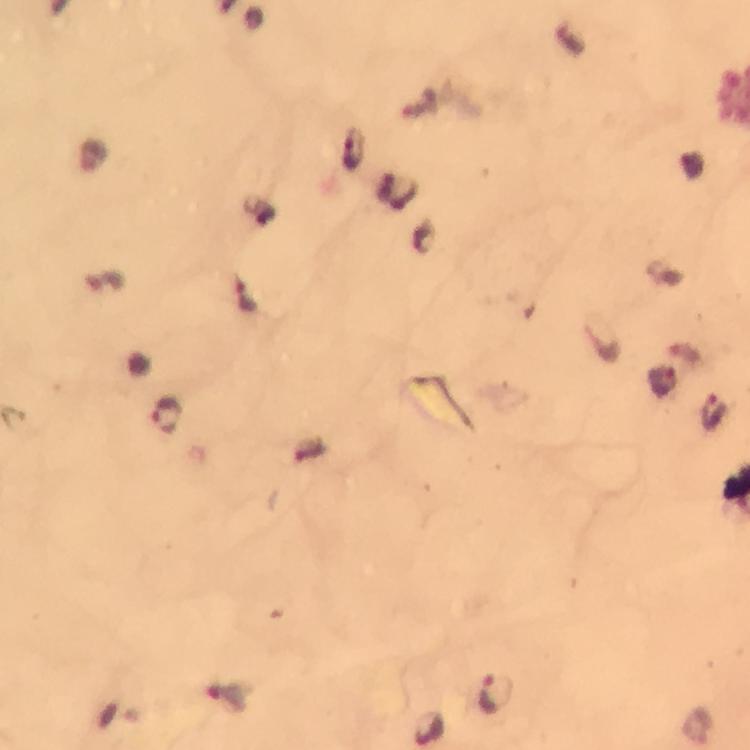
Approximate centers as (x, y) in pixels. Plasmodium parasite locations: (168, 413), (495, 691), (428, 726). Giemsa-stained preparation. Image is 750×750 pixels. Cropped region of a single field of view. Immersion oil was used. Smartphone photograph taken through a microscope. Thick smear. At 100x magnification. From a malaria diagnostic workup.